Comment on the morphology of the red blood cells.
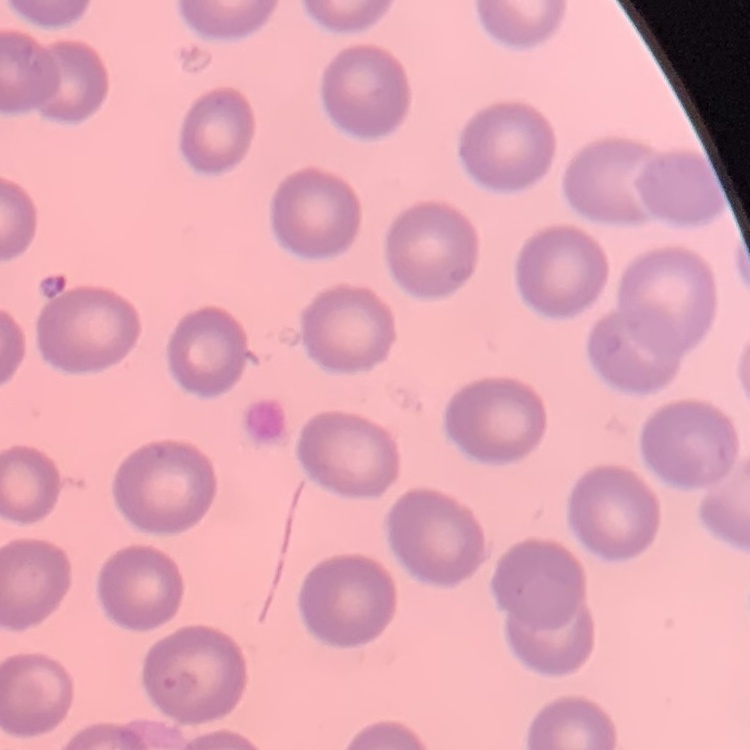
No rouleaux formation.

Summary:
  - Image type: one tile cut from a larger photomicrograph
  - Stain: Field's or Giemsa
  - Preparation: thin blood film